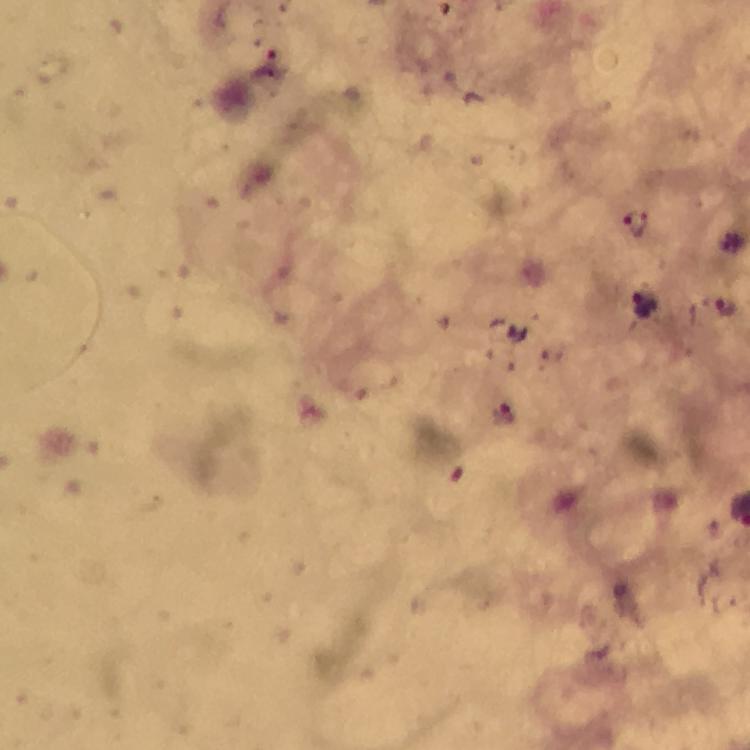
Approximate centers as {x, y} in pixels. Plasmodium parasite locations: {635, 225}, {724, 303}, {645, 308}, {501, 414}. Immersion oil applied. At 100x magnification. A crop from one field of view. From a diagnostic examination for malaria. Photographed with a smartphone mounted on the microscope. Thick blood film. Giemsa stain. Image is 750×750 pixels.